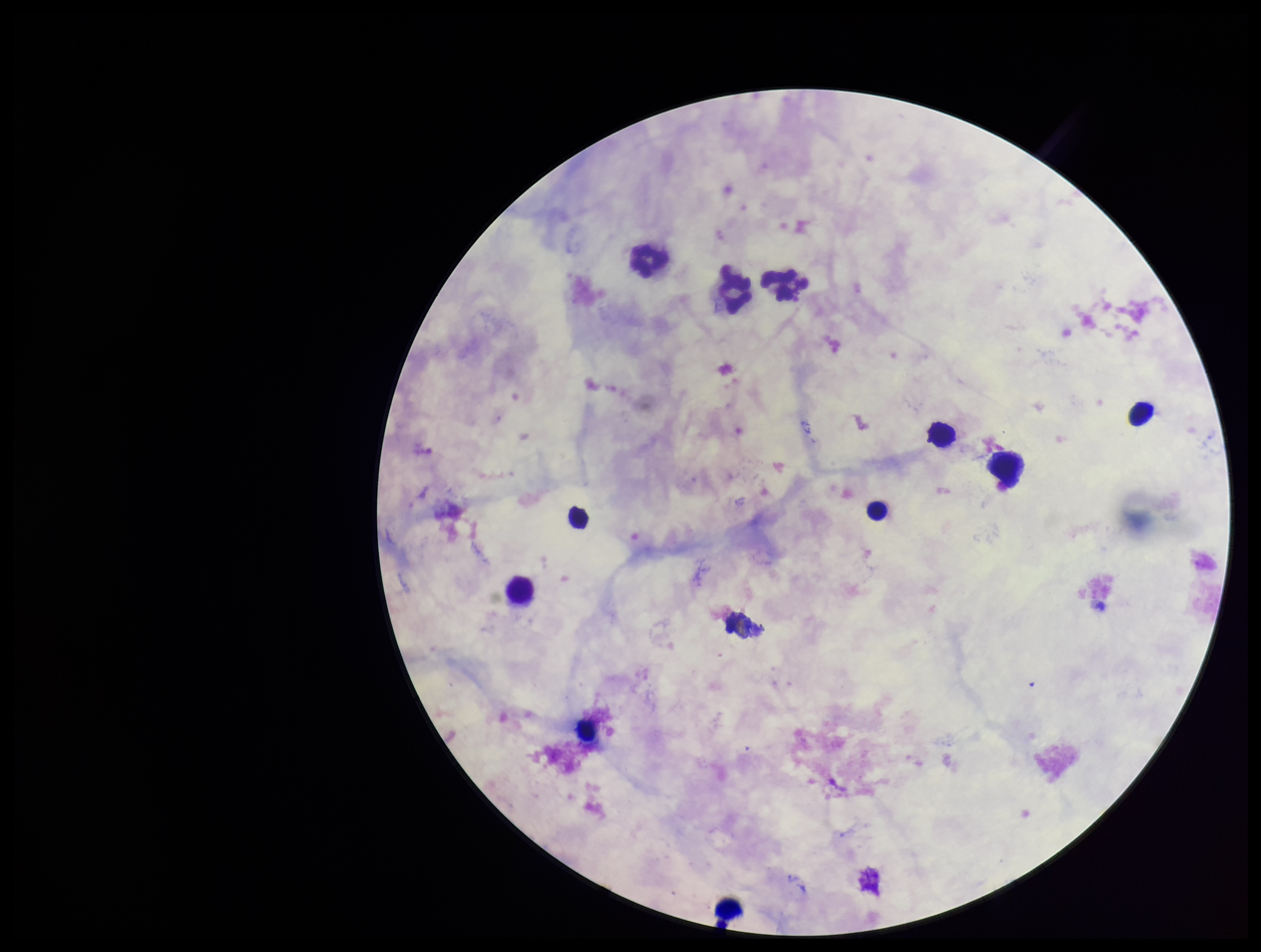

Plasmodium parasites: none identified. Giemsa stain. Preparation: thick blood smear. Photographed through the microscope eyepiece with a smartphone camera. Leukocyte count: 13. Parasite count: 0. Image is 1261×952 pixels. Patient malaria status: negative. Single field of view.